State which parasite is depicted.
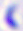

This is Toxoplasma gondii.

Summary:
  - Magnification: 400x
  - Modality: photomicrograph